Identify the parasite.
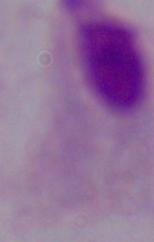

A trichomonad.

Photomicrograph. 1000x magnification.